State the blood parasite species.
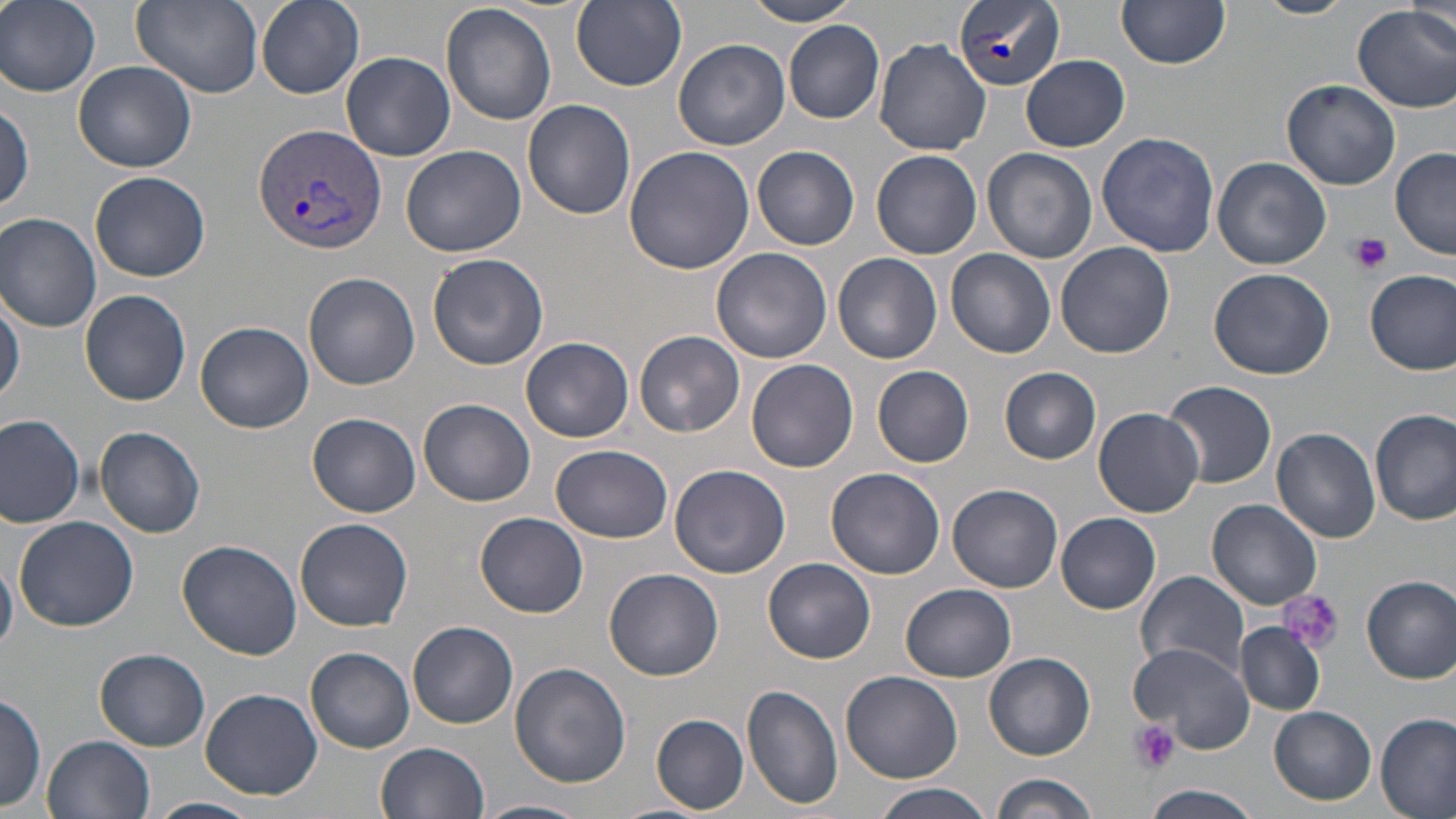

Plasmodium vivax.

platelet locations = approximate bounding boxes as named x1/y1/x2/y2 corners in pixels: (x1=1349, y1=232, x2=1391, y2=274), (x1=1279, y1=592, x2=1344, y2=654), (x1=1128, y1=720, x2=1179, y2=774)
field of view = single
image size = 1456×819 pixels
Plasmodium vivax-infected red blood cell locations = approximate bounding boxes as named x1/y1/x2/y2 corners in pixels: (x1=954, y1=0, x2=1065, y2=92), (x1=254, y1=123, x2=385, y2=253)
modality = light microscopy
stain = May-Grünwald-Giemsa
preparation = thin blood smear
uninfected red blood cell locations = approximate bounding boxes as named x1/y1/x2/y2 corners in pixels: (x1=1, y1=0, x2=101, y2=96), (x1=130, y1=0, x2=264, y2=97), (x1=258, y1=0, x2=364, y2=98), (x1=571, y1=0, x2=686, y2=92), (x1=744, y1=0, x2=862, y2=25), (x1=1252, y1=0, x2=1356, y2=19), (x1=1117, y1=1, x2=1230, y2=71), (x1=1354, y1=4, x2=1456, y2=113), (x1=441, y1=5, x2=557, y2=126), (x1=1407, y1=5, x2=1453, y2=49), (x1=782, y1=19, x2=885, y2=122), (x1=875, y1=38, x2=990, y2=155), (x1=674, y1=40, x2=788, y2=151), (x1=341, y1=51, x2=455, y2=162), (x1=1022, y1=55, x2=1129, y2=151), (x1=73, y1=61, x2=198, y2=172), (x1=1282, y1=78, x2=1401, y2=190), (x1=523, y1=99, x2=636, y2=219), (x1=0, y1=101, x2=33, y2=217), (x1=1097, y1=131, x2=1220, y2=257), (x1=402, y1=144, x2=526, y2=257), (x1=623, y1=146, x2=756, y2=275), (x1=752, y1=146, x2=860, y2=250), (x1=1390, y1=146, x2=1456, y2=259), (x1=983, y1=147, x2=1097, y2=263), (x1=871, y1=148, x2=982, y2=259), (x1=1213, y1=157, x2=1331, y2=271), (x1=89, y1=172, x2=210, y2=282), (x1=0, y1=213, x2=102, y2=332), (x1=1055, y1=242, x2=1176, y2=359), (x1=712, y1=248, x2=833, y2=364), (x1=946, y1=250, x2=1056, y2=359), (x1=831, y1=251, x2=943, y2=366), (x1=426, y1=253, x2=547, y2=372), (x1=1208, y1=267, x2=1335, y2=381), (x1=1366, y1=270, x2=1456, y2=374), (x1=303, y1=271, x2=421, y2=390), (x1=80, y1=289, x2=191, y2=405), (x1=1, y1=295, x2=24, y2=408), (x1=195, y1=321, x2=314, y2=433), (x1=634, y1=330, x2=745, y2=439), (x1=522, y1=336, x2=634, y2=442), (x1=746, y1=357, x2=859, y2=472), (x1=871, y1=366, x2=974, y2=467), (x1=1000, y1=367, x2=1102, y2=464), (x1=1163, y1=380, x2=1277, y2=489), (x1=418, y1=399, x2=537, y2=507), (x1=1094, y1=408, x2=1204, y2=518), (x1=1371, y1=410, x2=1456, y2=527), (x1=0, y1=412, x2=87, y2=528), (x1=309, y1=413, x2=420, y2=517), (x1=95, y1=425, x2=206, y2=538), (x1=1272, y1=428, x2=1380, y2=542), (x1=552, y1=443, x2=673, y2=542), (x1=669, y1=463, x2=791, y2=578), (x1=826, y1=467, x2=945, y2=580), (x1=948, y1=483, x2=1063, y2=593), (x1=1207, y1=498, x2=1323, y2=610), (x1=474, y1=511, x2=589, y2=617), (x1=1055, y1=511, x2=1161, y2=614), (x1=13, y1=516, x2=139, y2=632), (x1=294, y1=517, x2=413, y2=630), (x1=176, y1=538, x2=304, y2=660), (x1=0, y1=551, x2=19, y2=656), (x1=764, y1=558, x2=876, y2=664), (x1=604, y1=567, x2=725, y2=679), (x1=1135, y1=570, x2=1250, y2=679), (x1=1361, y1=573, x2=1456, y2=683), (x1=899, y1=584, x2=1016, y2=682), (x1=408, y1=622, x2=518, y2=727), (x1=1234, y1=623, x2=1324, y2=715), (x1=1128, y1=641, x2=1254, y2=751), (x1=96, y1=647, x2=211, y2=749), (x1=305, y1=647, x2=415, y2=753), (x1=985, y1=653, x2=1096, y2=760), (x1=509, y1=663, x2=631, y2=788), (x1=841, y1=670, x2=963, y2=783), (x1=742, y1=685, x2=843, y2=809), (x1=200, y1=687, x2=323, y2=801), (x1=0, y1=691, x2=47, y2=812), (x1=1269, y1=706, x2=1376, y2=802), (x1=649, y1=713, x2=751, y2=813), (x1=1376, y1=714, x2=1454, y2=819), (x1=44, y1=734, x2=155, y2=819), (x1=376, y1=741, x2=491, y2=819), (x1=990, y1=774, x2=1100, y2=819), (x1=871, y1=783, x2=996, y2=819), (x1=1145, y1=784, x2=1263, y2=819), (x1=148, y1=796, x2=260, y2=819), (x1=476, y1=798, x2=589, y2=819)
magnification = 1000x